Assess the morphology of the erythrocytes.
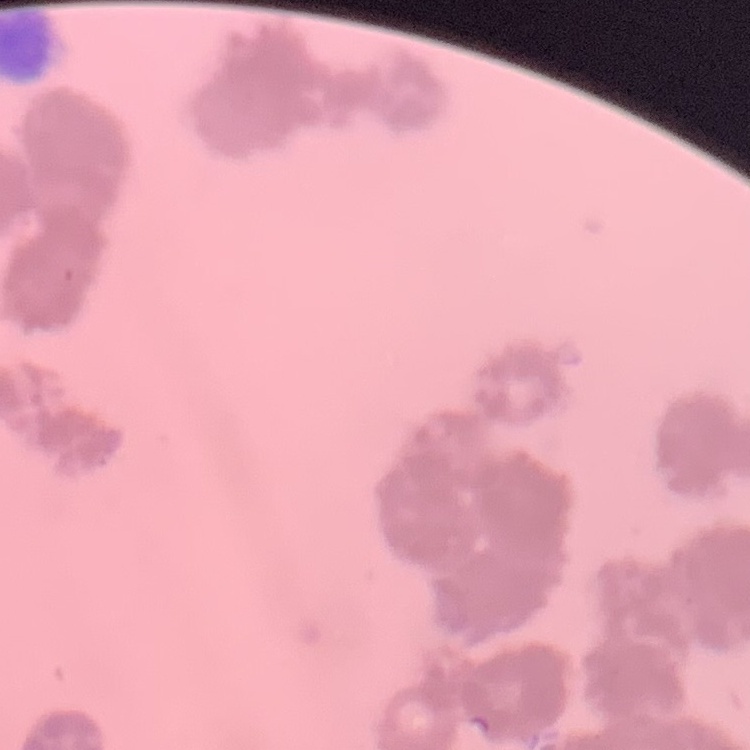
They show rouleaux formation.

Thin blood film. Stained with either Field's or Giemsa. Square crop of a larger photomicrograph.